Outline each blood parasite and name the species.
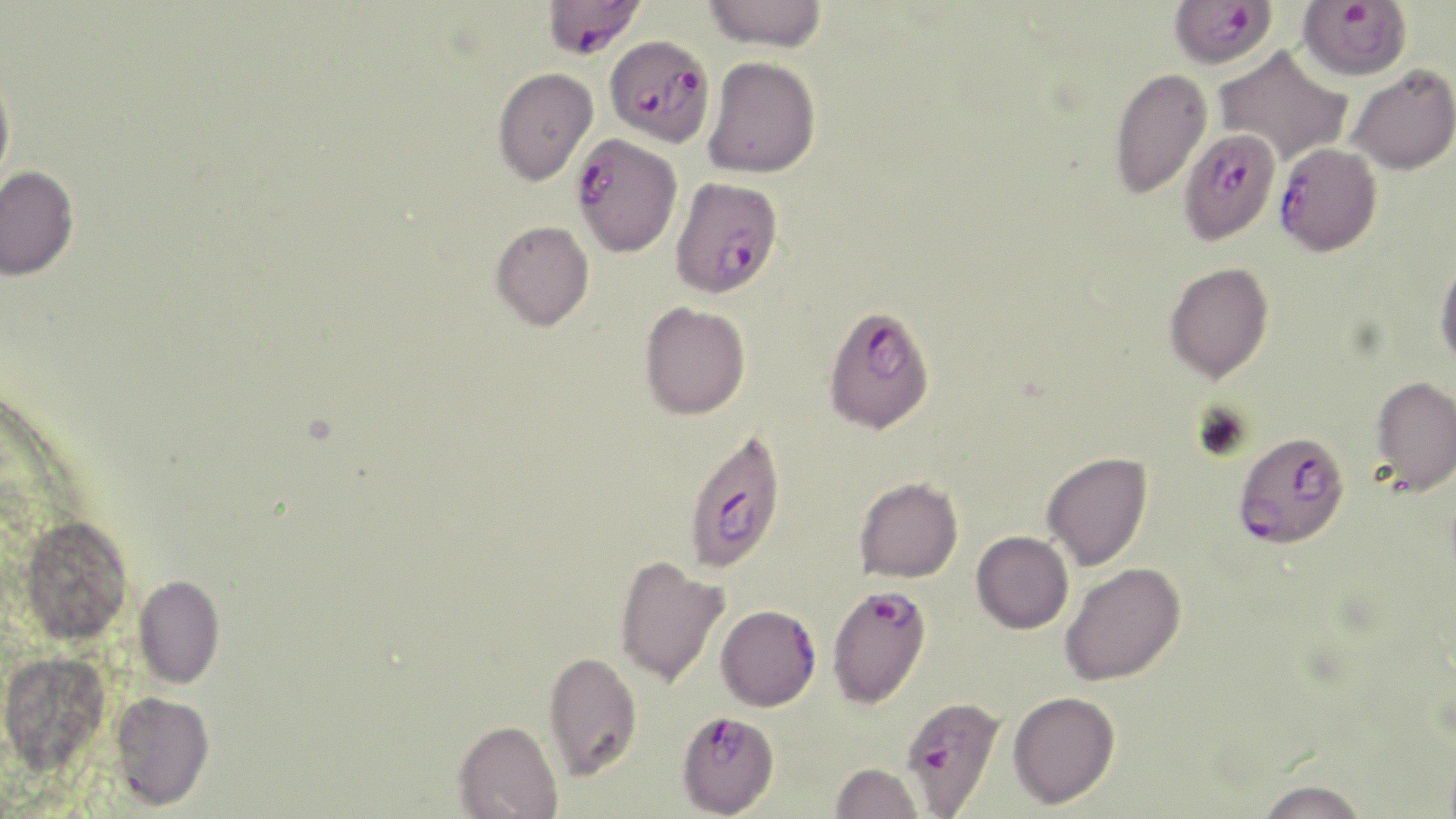

Approximate bounding boxes as (x1,y1)-(x2,y2) corner pairs in pixels.
Plasmodium falciparum-infected red blood cells: (543,0)-(647,59), (1297,0)-(1412,81), (1169,1)-(1276,69), (605,36)-(715,146), (1178,127)-(1281,245), (571,133)-(682,257), (1274,143)-(1382,257), (670,176)-(783,298), (822,304)-(935,433), (683,427)-(787,573), (1233,431)-(1350,549), (827,583)-(932,708), (715,605)-(821,711), (900,695)-(1005,816), (676,709)-(781,817).
No Plasmodium ovale, Plasmodium malariae, Plasmodium vivax, Babesia divergens, or Trypanosoma brucei observed.

slide_level_diagnosis: Plasmodium falciparum
magnification: 1000x
uninfected_red_blood_cell_locations: 'approximate bounding boxes as (x1,y1)-(x2,y2) corner pairs in pixels: (702,0)-(828,52), (1213,47)-(1353,167), (703,55)-(821,178), (0,64)-(15,196), (1346,65)-(1456,175), (492,67)-(598,186), (1108,67)-(1213,198), (0,166)-(79,281), (490,220)-(594,331), (1435,254)-(1456,370), (1165,261)-(1274,383), (639,301)-(751,420), (1371,376)-(1456,494), (1042,452)-(1153,571), (854,476)-(964,582), (18,515)-(133,645), (971,530)-(1073,633), (614,556)-(728,688), (1060,562)-(1186,686), (134,575)-(224,689), (543,649)-(643,780), (0,650)-(110,772), (1007,691)-(1120,808), (109,692)-(215,810), (454,719)-(563,818), (830,762)-(923,819), (1254,779)-(1370,819)'
field_of_view: one of a larger specimen
preparation: thin blood film
image_size: 1456×819 pixels
stain: May-Grünwald-Giemsa
modality: optical microscopy